Give the extent of all Plasmodium falciparum-infected red blood cells.
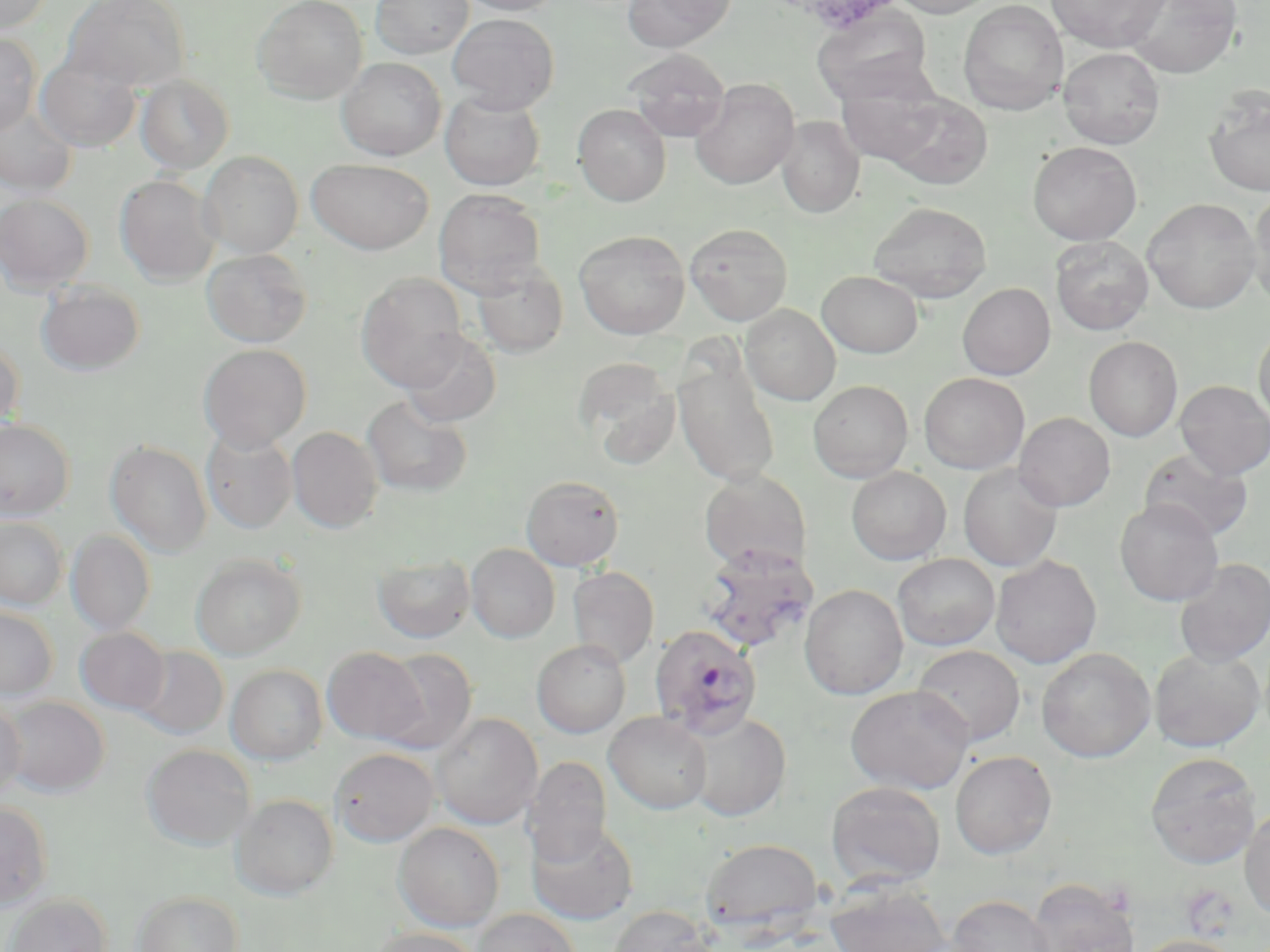
Approximate bounding boxes as (x1, y1, x2, y2) in pixels.
Plasmodium falciparum-infected red blood cells: (700, 545, 817, 653), (647, 624, 765, 738).

Uninfected red blood cell locations: (0, 0, 53, 34), (63, 0, 191, 91), (252, 0, 368, 104), (371, 0, 474, 59), (458, 0, 562, 15), (621, 0, 735, 51), (892, 0, 996, 18), (1045, 0, 1170, 52), (1125, 0, 1242, 78), (957, 1, 1069, 116), (812, 7, 933, 107), (448, 13, 559, 113), (0, 31, 41, 134), (1058, 47, 1166, 148), (622, 49, 731, 142), (35, 51, 141, 152), (337, 57, 446, 160), (834, 72, 946, 168), (135, 74, 234, 174), (690, 78, 800, 189), (1203, 86, 1270, 197), (440, 92, 545, 191), (881, 93, 993, 191), (573, 103, 671, 206), (0, 104, 78, 198), (776, 116, 865, 218), (1027, 141, 1142, 245), (198, 151, 303, 258), (307, 158, 433, 254), (114, 174, 221, 286), (433, 188, 546, 297), (1248, 189, 1270, 309), (0, 193, 94, 294), (1143, 198, 1261, 314), (868, 201, 992, 303), (684, 222, 793, 325), (574, 229, 691, 339), (1051, 236, 1153, 335), (202, 248, 312, 348), (472, 260, 568, 357), (817, 271, 923, 358), (356, 272, 469, 391), (36, 282, 145, 376), (957, 282, 1055, 380), (740, 305, 840, 405), (1254, 323, 1270, 428), (401, 331, 501, 427), (1084, 336, 1183, 442), (0, 337, 24, 434), (198, 344, 312, 451), (574, 358, 682, 469), (673, 361, 780, 487), (919, 372, 1029, 474), (808, 379, 914, 482), (1175, 380, 1270, 480), (362, 395, 473, 497), (1014, 412, 1116, 511), (0, 419, 74, 521), (287, 426, 384, 533), (201, 429, 297, 533), (106, 440, 213, 557), (1139, 448, 1253, 542), (958, 464, 1063, 571), (846, 466, 952, 564), (699, 469, 813, 574), (521, 475, 624, 571), (1115, 498, 1223, 606), (0, 516, 68, 610), (66, 530, 155, 635), (466, 544, 560, 642), (190, 552, 307, 659), (893, 553, 1000, 651), (372, 554, 475, 643), (990, 554, 1102, 668), (1174, 557, 1270, 667), (567, 566, 659, 668), (799, 584, 908, 700), (0, 605, 59, 699), (75, 627, 170, 715), (532, 639, 630, 738), (131, 645, 228, 740), (911, 645, 1025, 747), (322, 646, 428, 745), (1036, 647, 1156, 762), (378, 648, 478, 754), (1149, 648, 1265, 752), (226, 664, 327, 764), (845, 684, 974, 794), (2, 695, 109, 796), (0, 698, 27, 799), (605, 711, 712, 814), (683, 711, 791, 821), (431, 712, 543, 830), (142, 744, 256, 850), (329, 747, 439, 847), (949, 750, 1057, 859), (1146, 751, 1261, 868), (524, 756, 612, 867), (826, 781, 946, 888), (232, 793, 339, 899), (0, 800, 53, 908), (1240, 803, 1270, 921), (526, 819, 639, 925), (393, 822, 504, 932), (700, 837, 822, 935), (1028, 878, 1139, 952), (825, 879, 951, 952), (133, 890, 243, 952), (5, 894, 112, 952), (947, 894, 1056, 952), (606, 905, 717, 952), (471, 907, 582, 952), (368, 927, 483, 952), (1130, 934, 1244, 952). Slide-level diagnosis: Plasmodium falciparum. May-Grünwald-Giemsa stain. Single field of view. Captured at 1000x magnification. Thin blood smear. Image is 1270×952 pixels. Light microscopy.